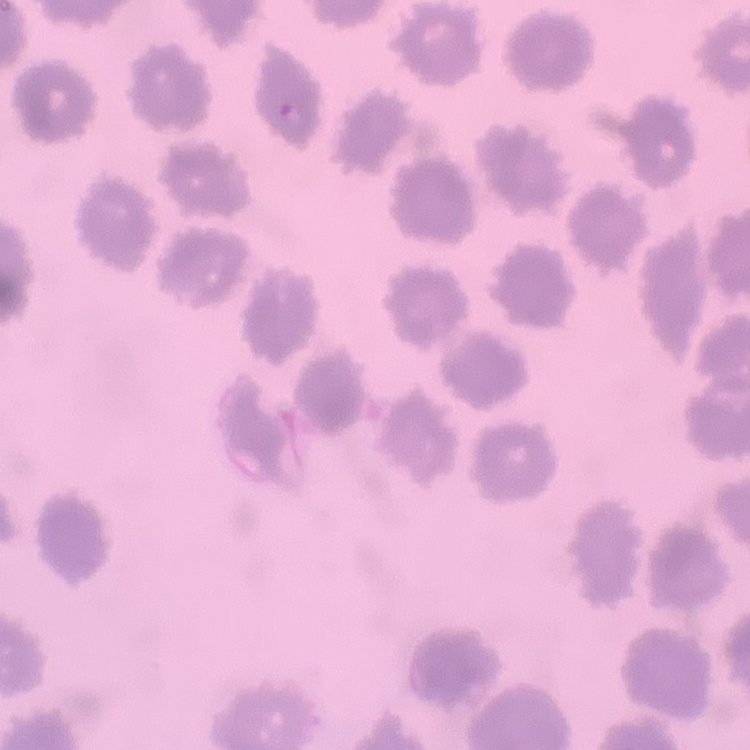
The red blood cells exhibit no rouleaux formation. Thin blood film. One tile cut from a larger photomicrograph. Stained with either Field's or Giemsa.